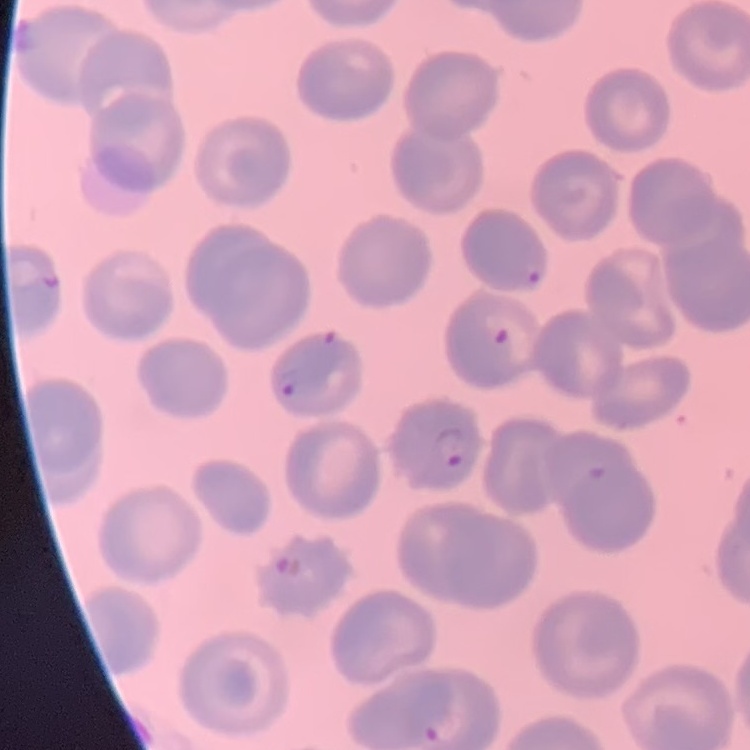
Summary:
  - Red blood cell morphology: no rouleaux formation
  - Image type: square crop of a larger photomicrograph
  - Stain: Field's or Giemsa
  - Preparation: thin peripheral smear